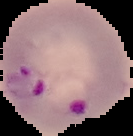
image type = segmented cell region on a black background
preparation = thin blood film
malaria status = parasitized
image size = 133×136 pixels